Comment on the morphology of the red blood cells.
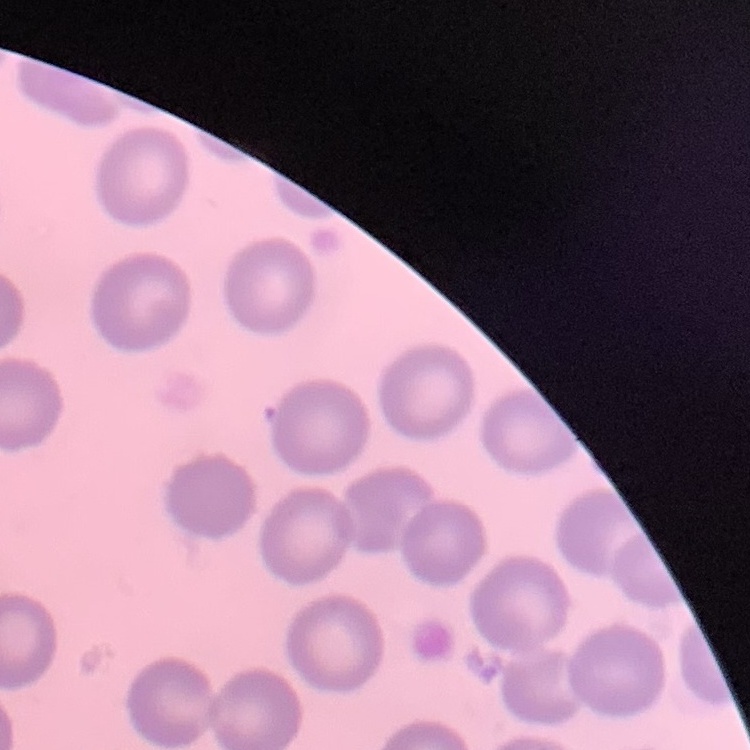

They show no rouleaux formation.

One tile cut from a larger photomicrograph. Field's or Giemsa stain. Thin blood film.